Comment on the morphology of the erythrocytes.
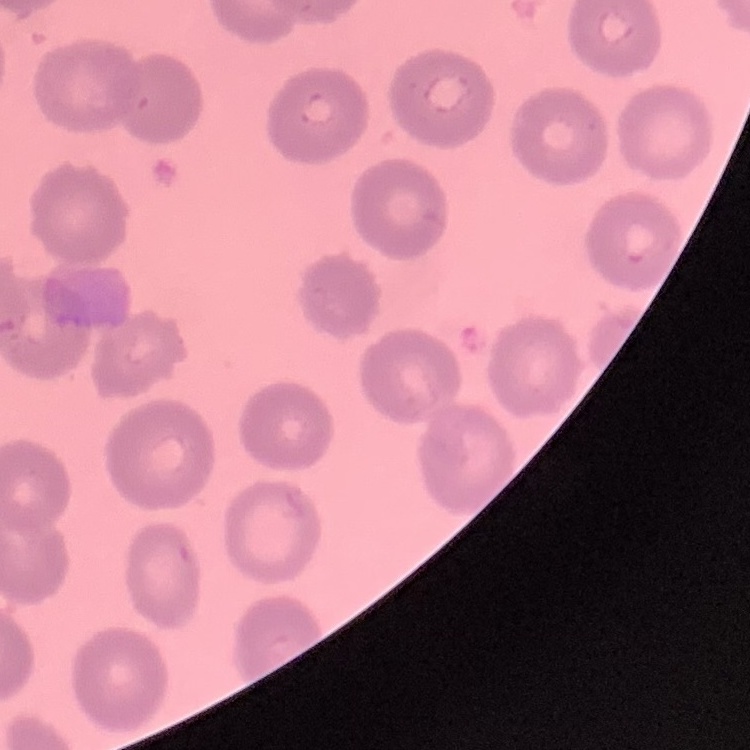
No rouleaux formation.

Square crop of a larger photomicrograph. Thin peripheral smear. Field's or Giemsa stain.